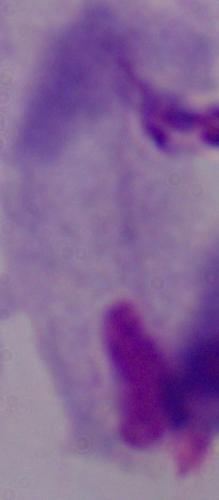

modality: micrograph
magnification: 1000x
identification: trichomonad